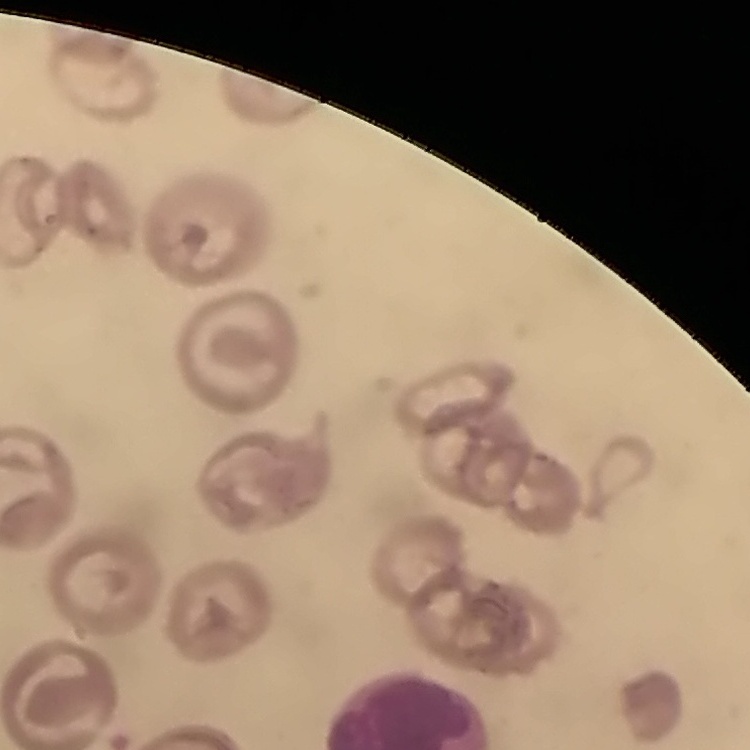

Summary:
  - Erythrocyte morphology: no rouleaux formation
  - Image type: one tile cut from a larger photomicrograph
  - Stain: Field's or Giemsa
  - Preparation: thin peripheral smear